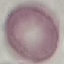

Summary:
  - Malaria status: uninfected
  - Image type: automatically extracted cell patch, resized to 64 × 64 pixels
  - Capture: smartphone through the microscope eyepiece
  - Stain: Giemsa
  - Preparation: thin blood film